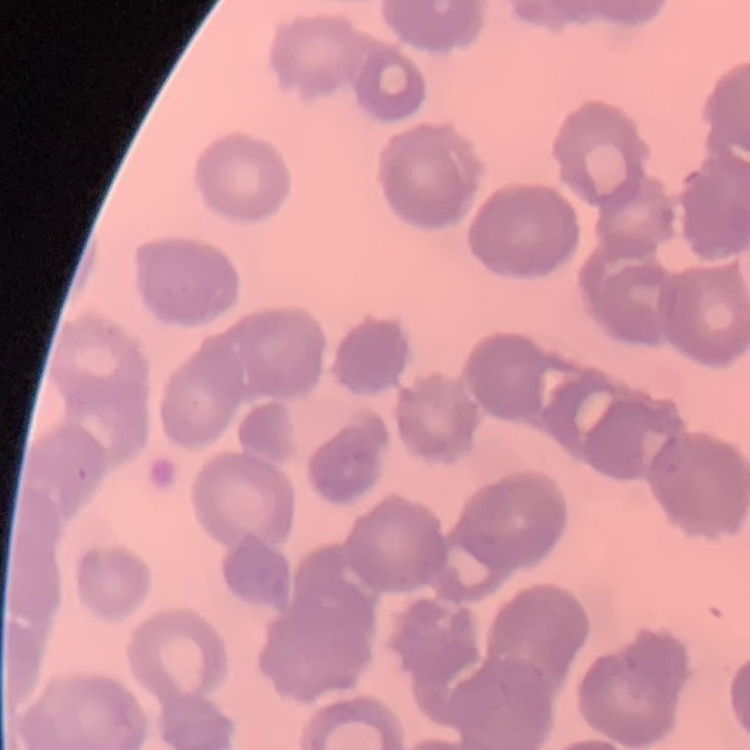

red_blood_cell_morphology: rouleaux formation
preparation: thin blood smear
image_type: one tile cut from a larger photomicrograph
stain: Field's or Giemsa